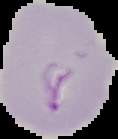
Summary:
  - Preparation: thin blood film
  - Image type: segmented cell region on a black background
  - Malaria status: parasitized
  - Image size: 118×139 pixels